Assess for malaria.
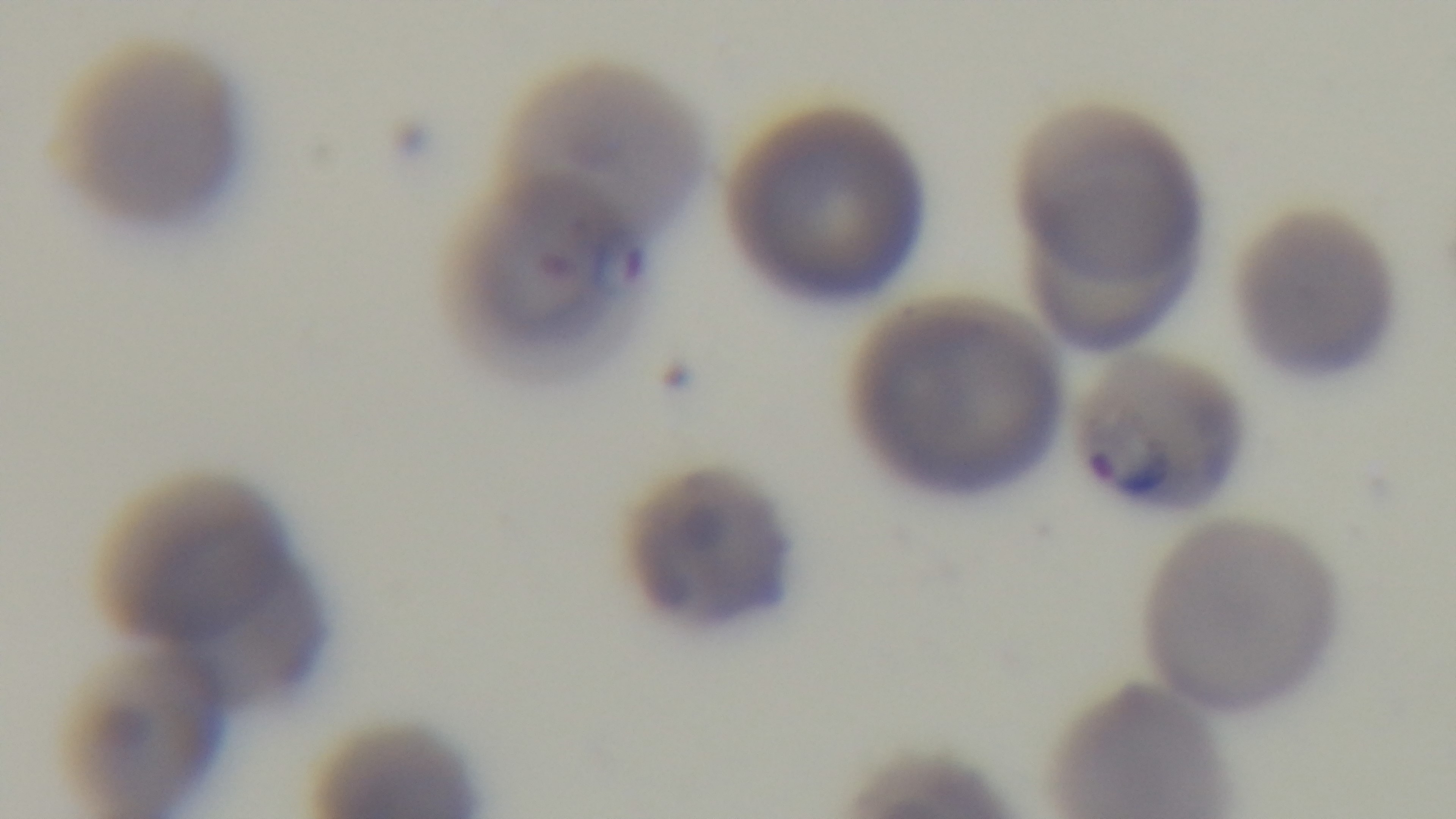
Positive.

Photomicrograph. Captured with a mounted 4K digital camera. Preparation: thin blood film. Giemsa stain. Single field of view. 100x oil-immersion objective.